Comment on the morphology of the red blood cells.
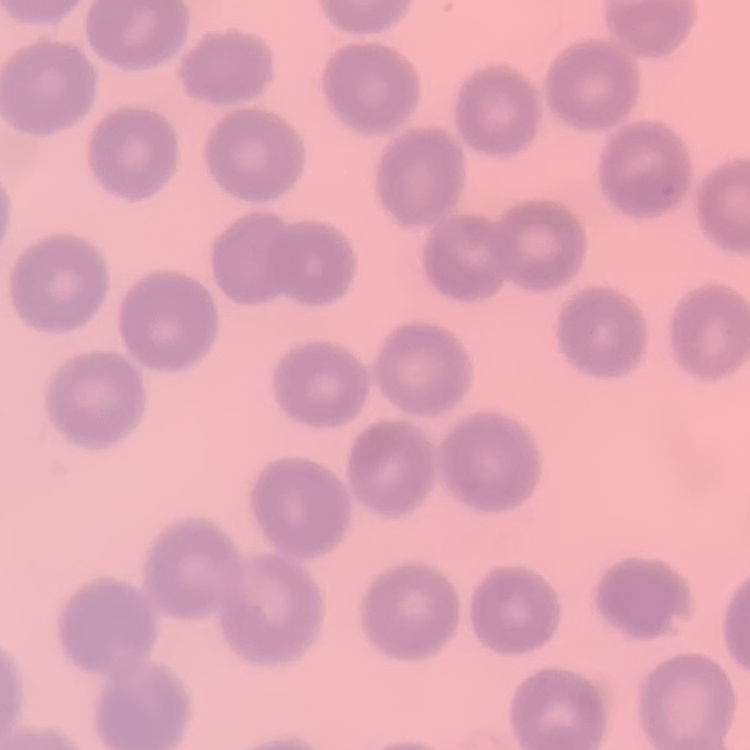
They show no rouleaux formation.

Summary:
  - Image type: square crop of a larger photomicrograph
  - Preparation: thin blood film
  - Stain: Field's or Giemsa